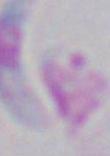
Summary:
  - Identification: Toxoplasma gondii
  - Magnification: 1000x
  - Modality: micrograph